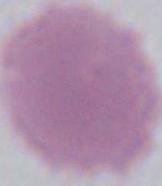

identification = red blood cell
modality = micrograph
magnification = 1000x